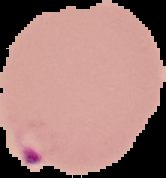

{
  "image_type": "cell region segmented out of the field of view; surrounding area masked to black",
  "malaria_status": "parasitized",
  "image_size": "166×178 pixels",
  "preparation": "thin blood film"
}